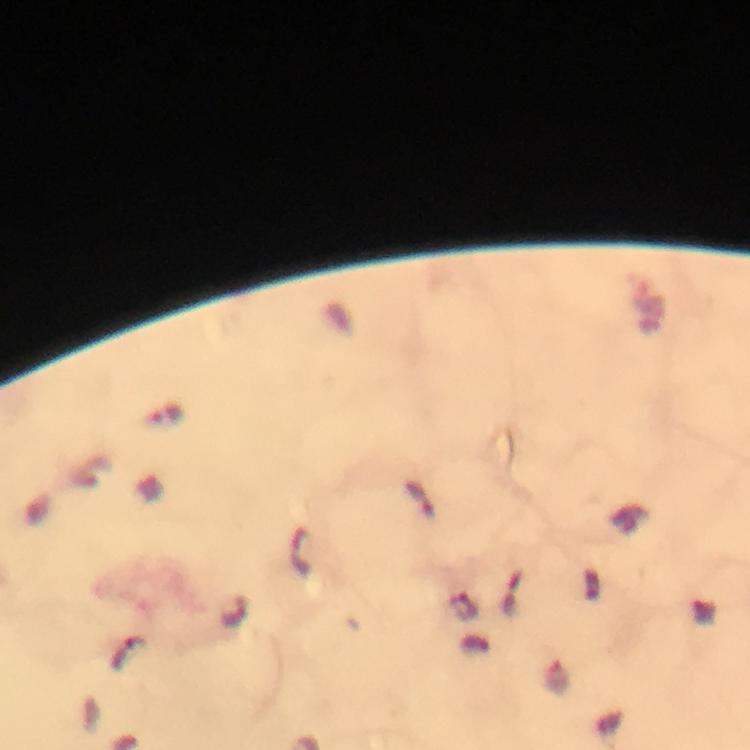

preparation = thick blood film
context = from a diagnostic examination for malaria
capture = smartphone photograph through a microscope
stain = Giemsa
magnification = 100x
image size = 750×750 pixels
cropped from = a single field of view
immersion oil = applied
Plasmodium parasite locations = approximate centers as {x, y} in pixels: {463, 607}, {126, 653}